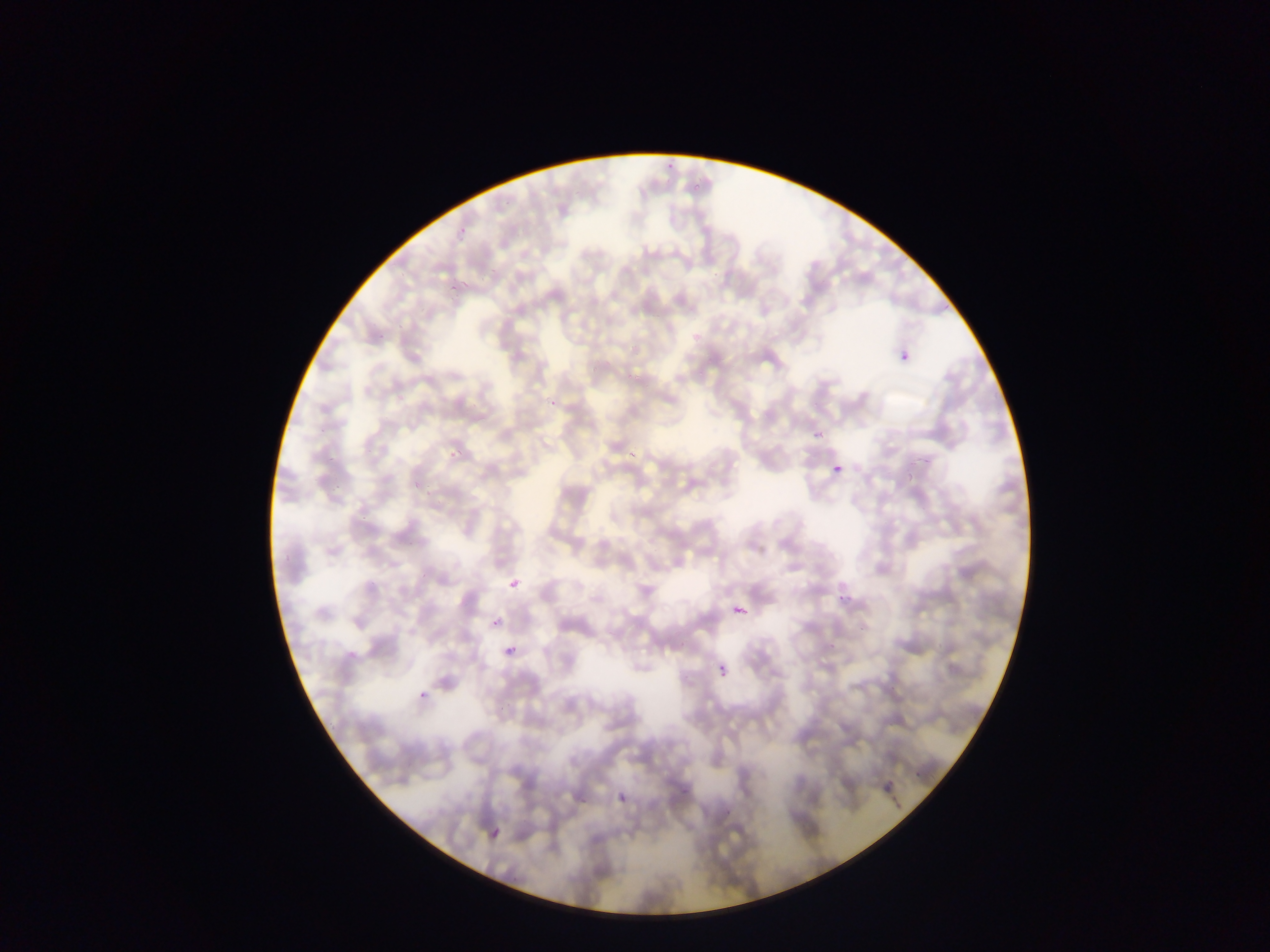

country = Ghana
capture = mobile-phone photograph through a microscope
preparation = thin blood film
malaria parasite locations = approximate bounding boxes as [left, top, right, bottom] in pixels: [898, 346, 922, 368], [828, 461, 849, 476], [502, 578, 522, 592], [730, 602, 746, 618], [489, 613, 507, 627], [501, 638, 516, 655], [717, 650, 729, 678], [416, 680, 432, 705], [881, 769, 898, 794], [603, 790, 627, 802], [484, 821, 502, 845]
image size = 1270×952 pixels
field of view = single